Locate every leukocyte (white blood cell).
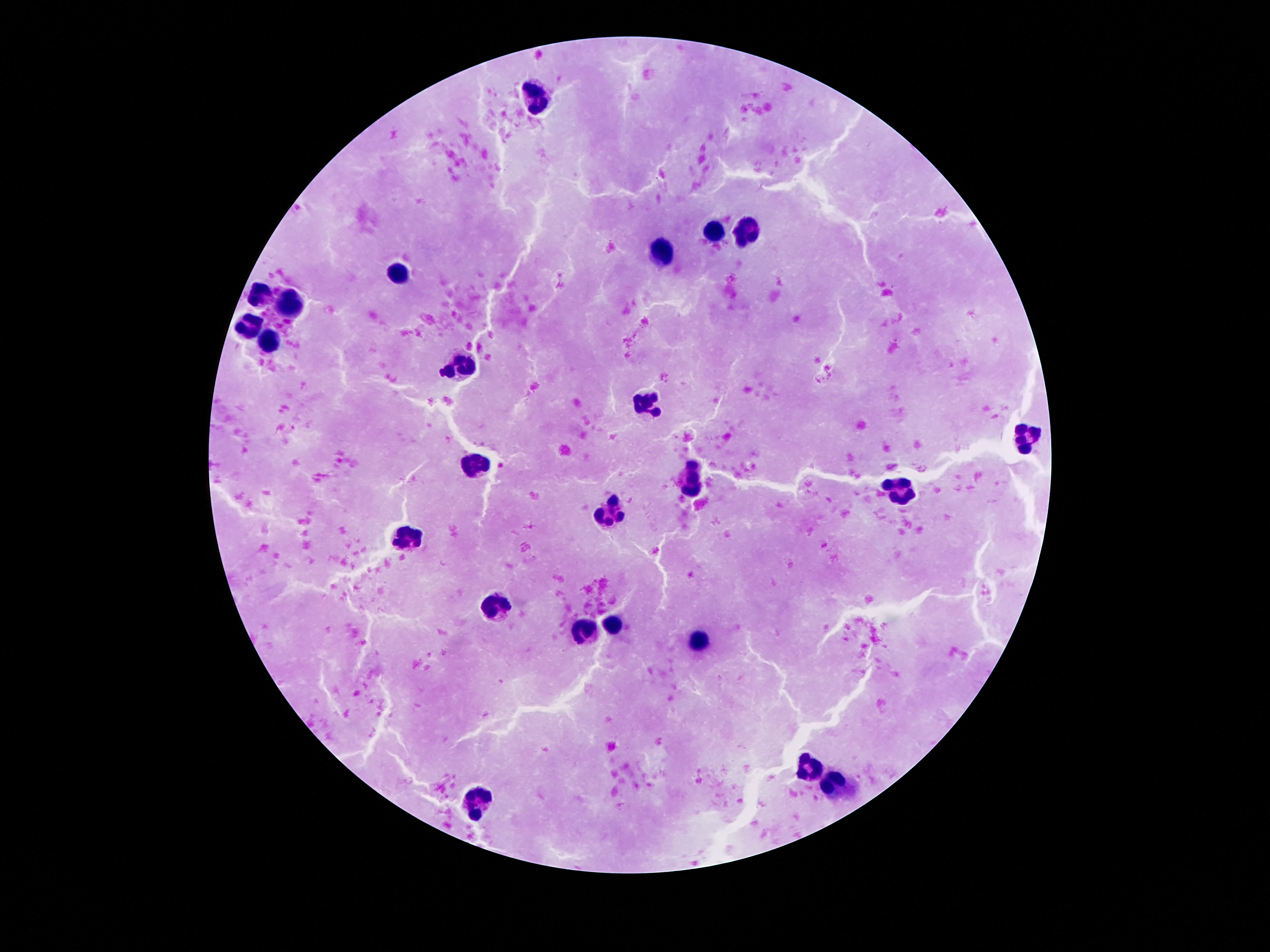

Approximate centers as {x, y} in pixels.
Leukocytes: {535, 97}, {714, 230}, {752, 231}, {661, 252}, {401, 270}, {262, 294}, {290, 305}, {248, 325}, {273, 346}, {460, 367}, {644, 405}, {1027, 438}, {472, 466}, {693, 477}, {896, 490}, {611, 514}, {404, 540}, {495, 609}, {611, 626}, {581, 631}, {698, 638}, {808, 772}, {835, 784}, {478, 798}.

Summary:
  - Patient malaria status: negative
  - Stain: Giemsa
  - Capture: smartphone camera through the microscope eyepiece
  - Field of view: single
  - Preparation: thick peripheral-blood smear
  - Magnification: 100x
  - Image size: 1270×952 pixels